Locate and identify every blood parasite.
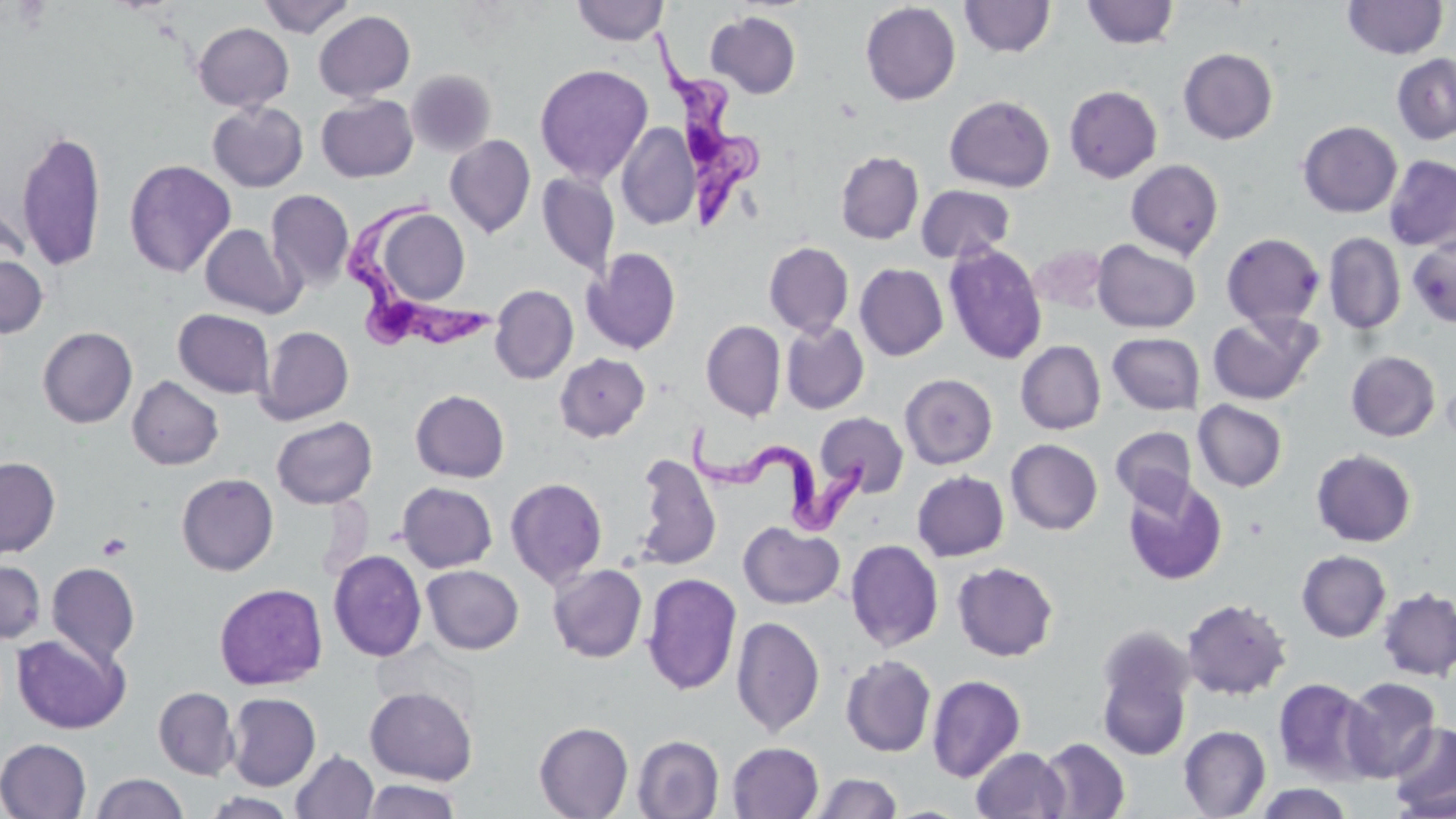

Approximate bounding boxes as (x1,y1)-(x2,y2) corner pairs in pixels.
Trypanosoma brucei: (652,27)-(761,231), (347,194)-(495,356), (686,423)-(867,541).
No Plasmodium falciparum, Plasmodium ovale, Plasmodium malariae, Plasmodium vivax, or Babesia divergens observed.

Uninfected red blood cell locations: (257,0)-(356,38), (571,0)-(669,45), (1342,0)-(1448,59), (960,1)-(1056,58), (1081,1)-(1180,49), (860,2)-(961,106), (705,10)-(802,99), (314,11)-(415,101), (193,22)-(293,112), (1178,48)-(1278,144), (1392,54)-(1456,144), (533,63)-(654,184), (406,69)-(497,158), (1064,85)-(1163,183), (316,95)-(418,182), (944,95)-(1055,192), (208,101)-(309,192), (1297,121)-(1402,218), (616,122)-(700,230), (15,127)-(108,272), (445,135)-(536,238), (835,150)-(924,244), (1383,155)-(1456,251), (124,159)-(236,278), (1125,159)-(1224,260), (536,173)-(620,278), (916,184)-(1015,263), (265,189)-(355,293), (0,196)-(33,276), (372,207)-(471,307), (200,224)-(303,319), (1323,232)-(1406,334), (1221,233)-(1325,329), (1407,237)-(1456,328), (1092,239)-(1200,333), (763,241)-(854,338), (943,243)-(1048,364), (1028,245)-(1107,314), (582,248)-(682,354), (0,251)-(48,338), (854,263)-(949,361), (490,284)-(578,384), (173,309)-(275,399), (1207,312)-(1321,405), (701,320)-(786,421), (781,320)-(869,414), (257,325)-(354,425), (37,326)-(137,428), (1108,332)-(1204,415), (1015,340)-(1106,435), (1346,350)-(1441,441), (555,353)-(650,442), (900,373)-(997,469), (127,375)-(224,470), (410,389)-(510,482), (1193,400)-(1287,491), (815,411)-(909,497), (271,416)-(377,509), (1111,426)-(1196,511), (1006,439)-(1103,535), (1311,448)-(1417,547), (633,452)-(722,572), (0,456)-(60,557), (911,470)-(1009,561), (176,473)-(278,576), (1122,476)-(1228,586), (505,477)-(608,588), (396,482)-(498,573), (738,521)-(845,609), (845,539)-(944,652), (328,549)-(426,661), (1296,550)-(1391,642), (0,559)-(46,643), (952,561)-(1059,661), (46,562)-(140,666), (548,564)-(648,663), (421,565)-(524,654), (642,573)-(742,695), (214,583)-(328,690), (1377,587)-(1456,681), (1182,597)-(1292,700), (731,615)-(825,737), (1095,629)-(1195,761), (13,633)-(129,734), (840,655)-(936,757), (927,674)-(1026,783), (1273,677)-(1375,784), (1340,677)-(1441,781), (364,685)-(478,785), (153,686)-(240,780), (226,692)-(321,790), (534,721)-(634,819), (1388,721)-(1456,817), (1178,725)-(1271,818), (633,735)-(724,819), (1036,737)-(1131,819), (0,738)-(91,818), (727,742)-(824,818), (971,747)-(1070,819), (291,749)-(379,819), (810,772)-(902,818), (91,773)-(188,819), (360,778)-(463,819), (1251,783)-(1356,818), (200,792)-(300,818). Platelet locations: (97,534)-(132,561). Slide-level diagnosis: Trypanosoma brucei. Light microscopy. Thin blood film. Captured at 1000x magnification. Image is 1456×819 pixels. One field of a larger specimen. May-Grünwald-Giemsa-stained preparation.